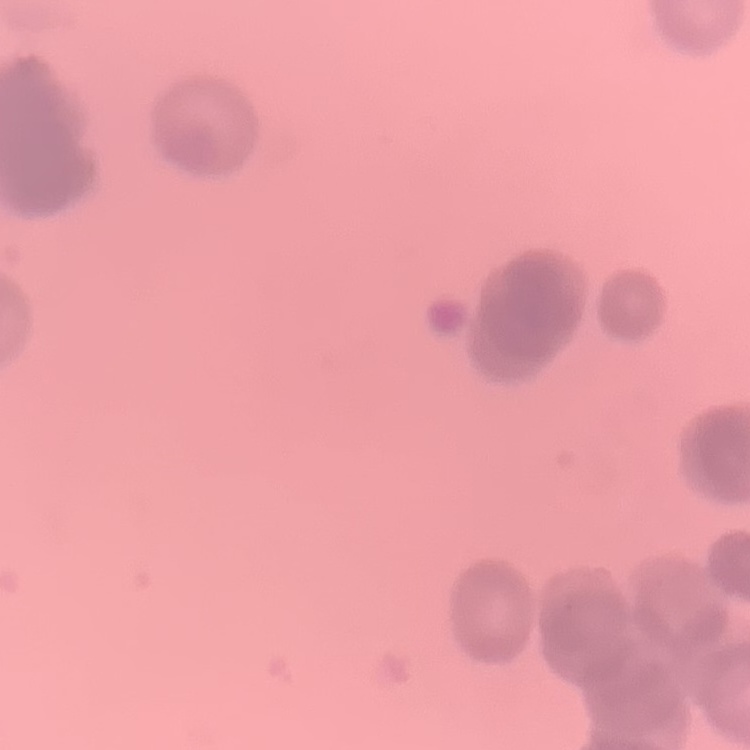

The red blood cells show rouleaux formation. Thin peripheral smear. Square crop of a larger photomicrograph. Field's or Giemsa stain.